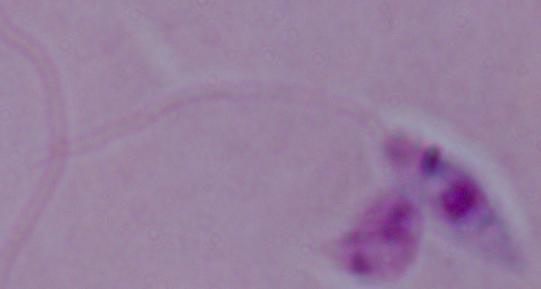
{
  "identification": "Leishmania",
  "modality": "photomicrograph",
  "magnification": "1000x"
}